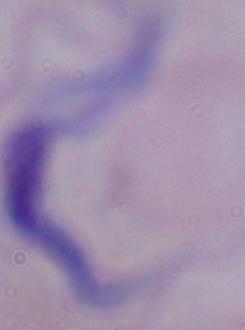

identification = trypanosome
magnification = 1000x
modality = micrograph